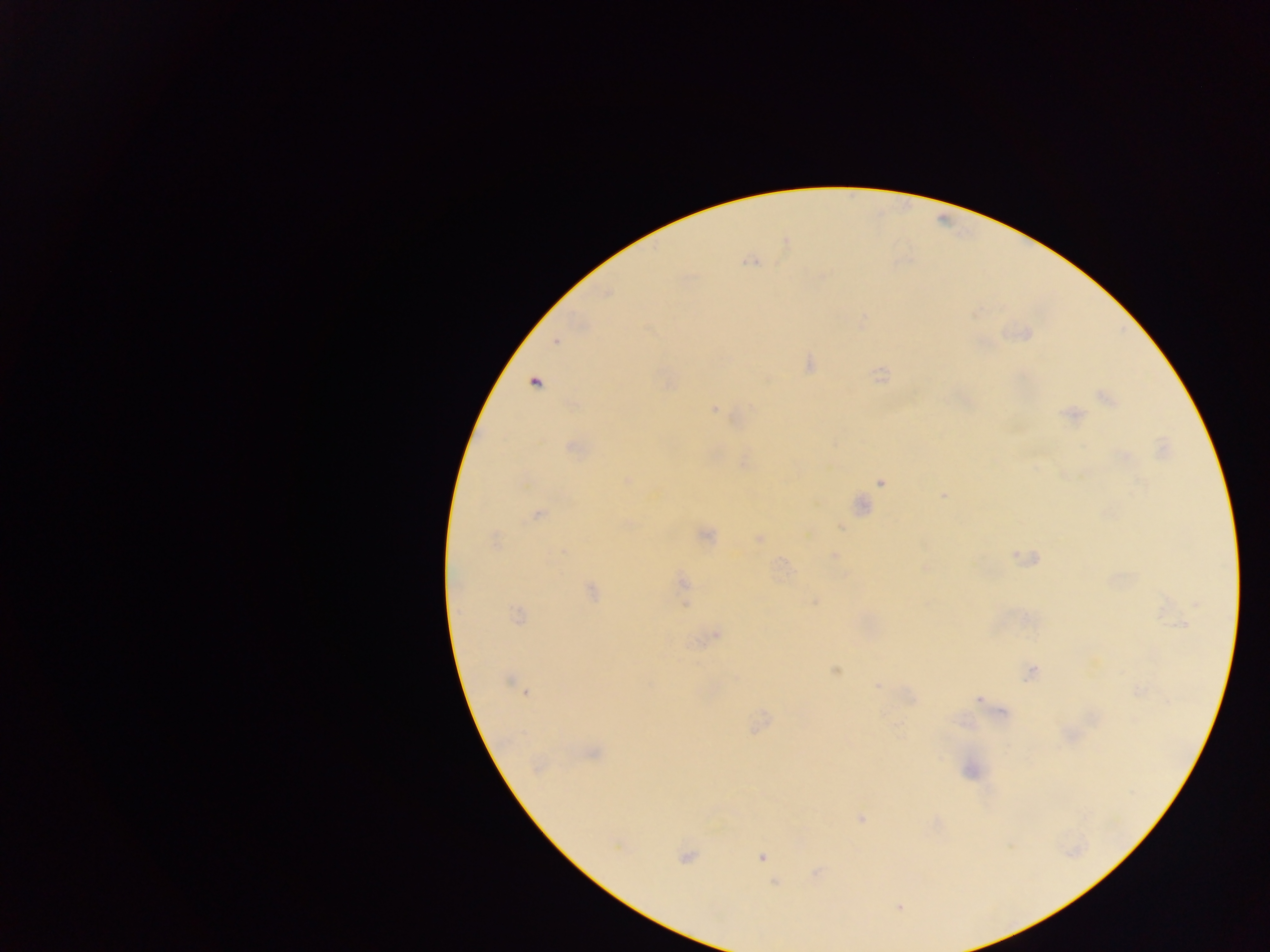
Approximate centers as {x, y} in pixels. Plasmodium parasite locations: {751, 261}, {862, 322}, {1026, 333}, {557, 341}, {808, 363}, {881, 374}, {535, 382}, {1105, 397}, {714, 407}, {1072, 414}, {572, 447}, {744, 463}, {626, 480}, {880, 482}, {943, 495}, {860, 505}, {537, 513}, {839, 525}, {704, 535}, {758, 539}, {495, 541}, {833, 556}, {1025, 558}, {925, 566}, {681, 582}, {590, 590}, {815, 602}, {684, 603}, {516, 615}, {716, 634}, {835, 670}, {1031, 672}, {511, 682}, {877, 684}, {525, 691}, {979, 699}, {759, 723}, {592, 752}, {538, 767}, {970, 770}, {861, 818}, {685, 857}, {761, 857}, {816, 873}, {775, 883}, {899, 906}. Photographed through a microscope with a mobile-phone camera. Thick blood film. Sample from Ghana. One field of view. Image is 1270×952 pixels.